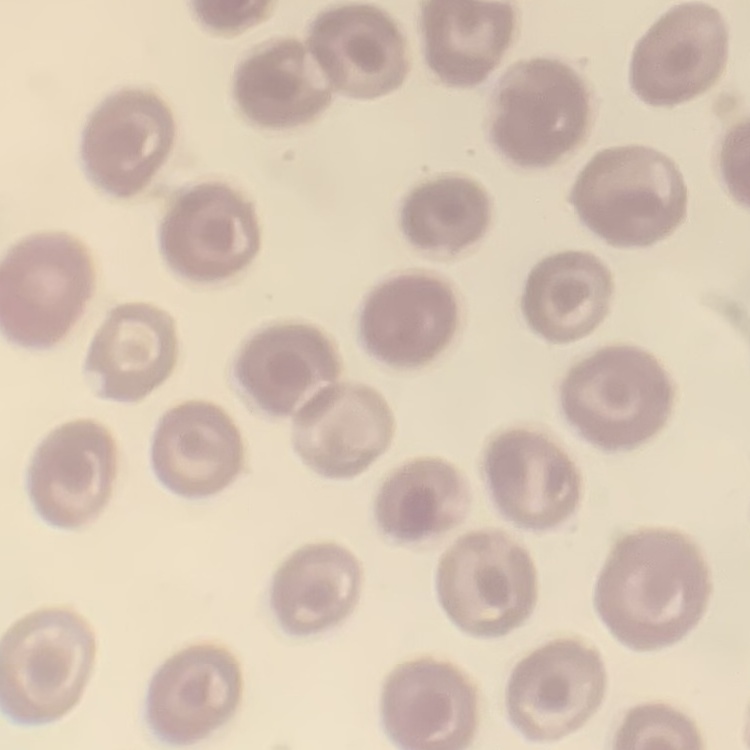

The erythrocytes show no rouleaux formation. Square crop of a larger photomicrograph. Field's or Giemsa stain. Thin blood smear.